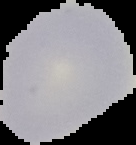

Result: no Plasmodium parasites detected. Image is 136×145 pixels. From a thin blood film. Cell region segmented out of the field of view; the surrounding area is masked to black.